State which parasite is depicted.
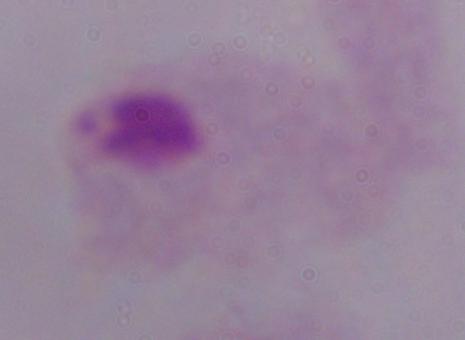
A trichomonad.

Summary:
  - Modality: photomicrograph
  - Magnification: 1000x